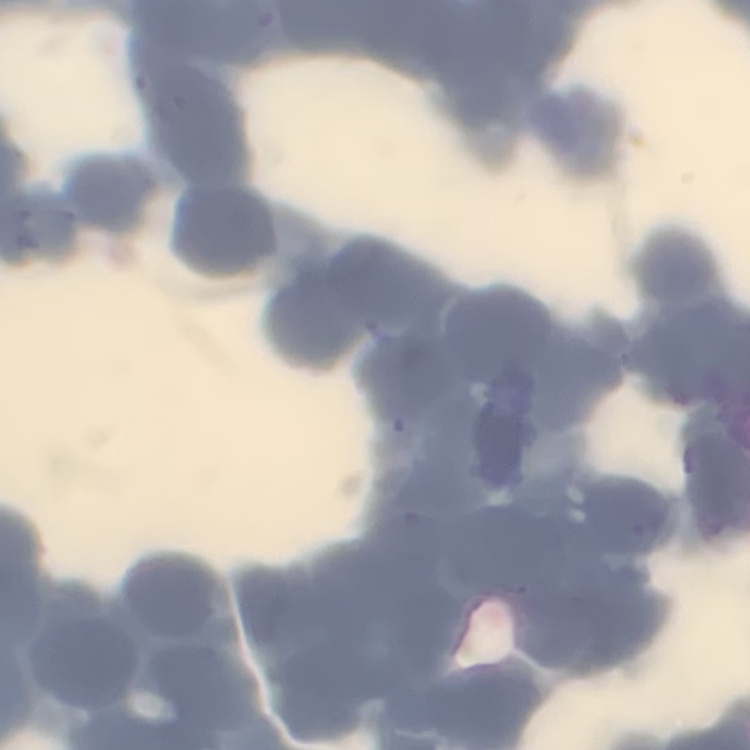

erythrocyte morphology = rouleaux formation
image type = square crop of a larger photomicrograph
preparation = thin peripheral smear
stain = Field's or Giemsa